Name the blood parasite species.
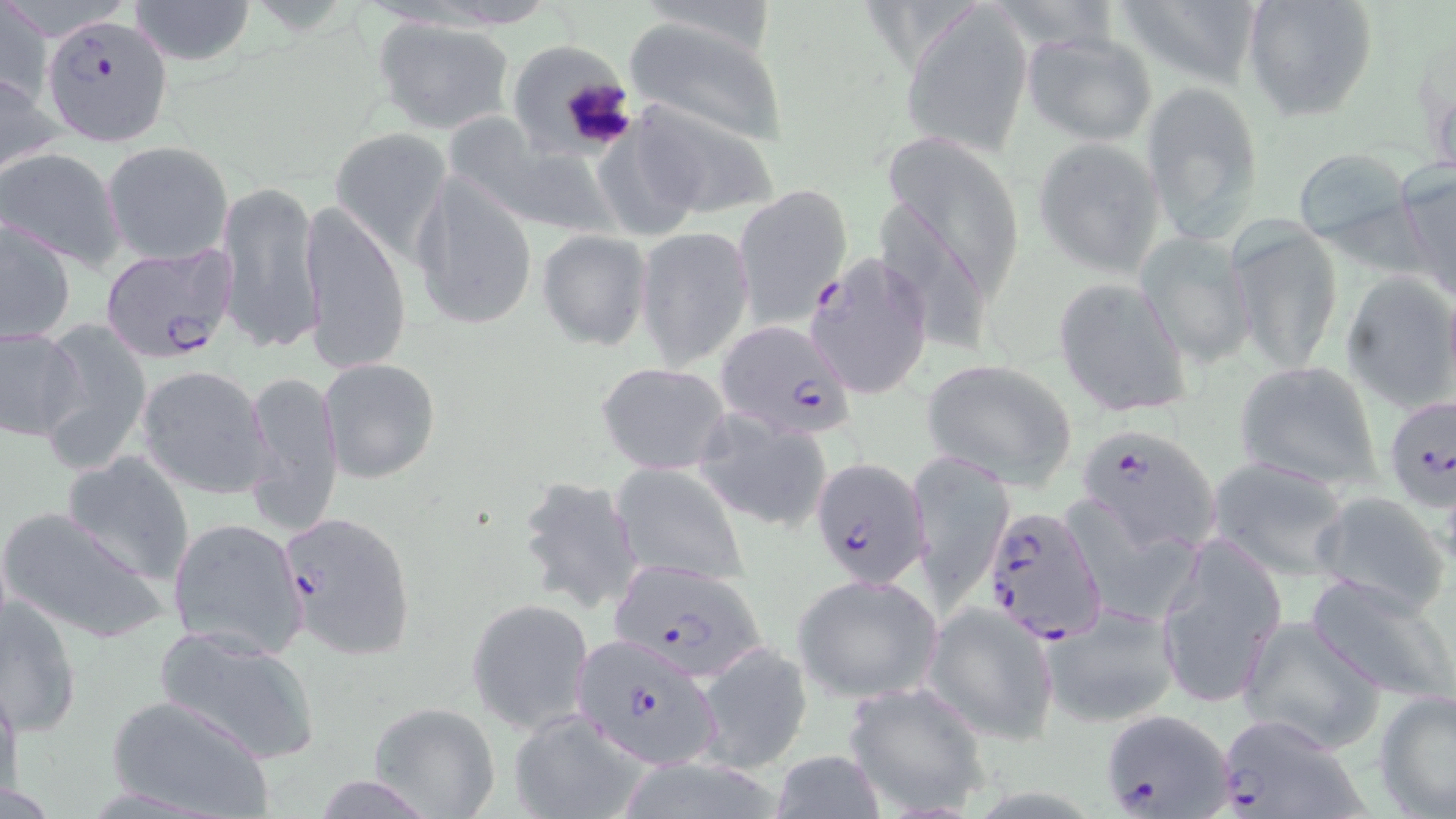

Plasmodium falciparum.

Summary:
  - Coordinate format: approximate bounding boxes as (x1, y1, x2, y2) in pixels
  - Uninfected red blood cell locations: (2, 0, 51, 110), (127, 0, 257, 67), (1112, 0, 1265, 89), (1242, 0, 1380, 122), (904, 2, 1033, 158), (624, 15, 786, 145), (371, 16, 517, 133), (1021, 30, 1159, 145), (513, 40, 646, 150), (0, 69, 60, 178), (1140, 78, 1264, 242), (629, 99, 779, 219), (457, 111, 629, 236), (331, 128, 451, 258), (881, 132, 1024, 316), (593, 133, 716, 244), (1033, 138, 1166, 277), (103, 141, 233, 264), (1291, 146, 1416, 251), (0, 147, 125, 271), (1396, 162, 1456, 302), (409, 169, 540, 330), (216, 179, 322, 353), (731, 184, 850, 327), (874, 194, 994, 357), (300, 201, 411, 380), (2, 219, 76, 342), (1228, 223, 1342, 374), (635, 226, 755, 370), (537, 229, 652, 350), (1139, 234, 1258, 367), (1341, 272, 1456, 412), (1052, 276, 1193, 419), (34, 319, 153, 472), (0, 324, 85, 440), (317, 356, 442, 485), (921, 359, 1077, 487), (1233, 360, 1383, 492), (596, 361, 733, 475), (136, 364, 274, 499), (243, 367, 345, 538), (692, 406, 833, 535), (62, 453, 197, 584), (908, 455, 1010, 613), (1206, 456, 1354, 578), (611, 463, 749, 587), (515, 475, 646, 618), (1309, 489, 1450, 614), (0, 505, 168, 645), (168, 516, 308, 659), (1156, 539, 1285, 708), (1304, 572, 1456, 703), (792, 574, 943, 703), (0, 597, 82, 735), (467, 597, 594, 734), (1042, 601, 1181, 728), (923, 602, 1058, 742), (1237, 616, 1387, 754), (154, 624, 322, 765), (694, 642, 814, 775), (0, 674, 21, 812), (849, 682, 994, 818), (1376, 686, 1456, 819), (103, 694, 276, 819), (365, 701, 501, 819), (506, 707, 649, 819), (769, 750, 886, 819)
  - Plasmodium falciparum-infected red blood cell locations: (44, 14, 174, 147), (99, 244, 235, 362), (798, 251, 933, 400), (715, 320, 858, 441), (1382, 392, 1456, 511), (1080, 424, 1221, 556), (811, 457, 932, 588), (980, 503, 1106, 645), (278, 509, 417, 663), (603, 558, 770, 683), (566, 634, 730, 770), (1099, 709, 1236, 816), (1211, 711, 1372, 819)
  - Platelet locations: (558, 76, 637, 150)
  - Modality: light microscopy
  - Preparation: thin blood smear
  - Stain: May-Grünwald-Giemsa
  - Magnification: 1000x
  - Field of view: one of a larger specimen
  - Image size: 1456×819 pixels